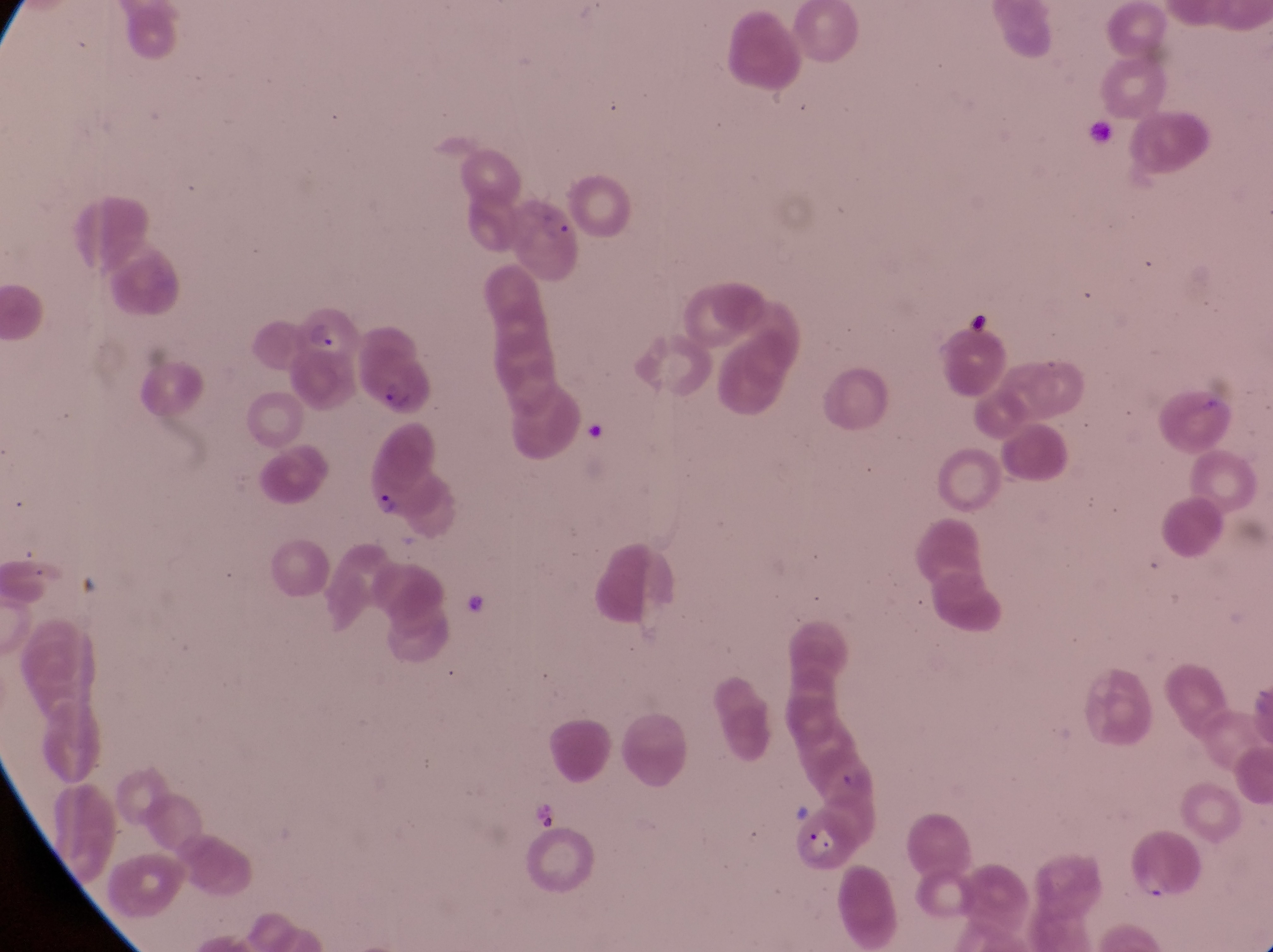

Approximate bounding boxes as {left, top, right, bottom} in pixels. Parasitised red blood cell locations: {511, 192, 585, 282}, {292, 305, 357, 360}, {359, 334, 436, 421}, {359, 430, 442, 527}, {792, 812, 859, 875}. Artifact (platelet-like body, stain precipitate, or debris) locations: {964, 310, 991, 337}. Image is 1273×952 pixels. Collected in Uganda. Photographed through the eyepiece of an Olympus CX-23 microscope with a smartphone camera. At a magnification of 1000x. Single field of view. Thin blood smear.